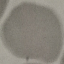 Malaria status: uninfected. Photographed with a smartphone camera at the microscope eyepiece. Giemsa stain. Thin smear of blood. Cell patch, automatically extracted from a larger field of view and resized to 64 × 64 pixels.